Assess the morphology of the red blood cells.
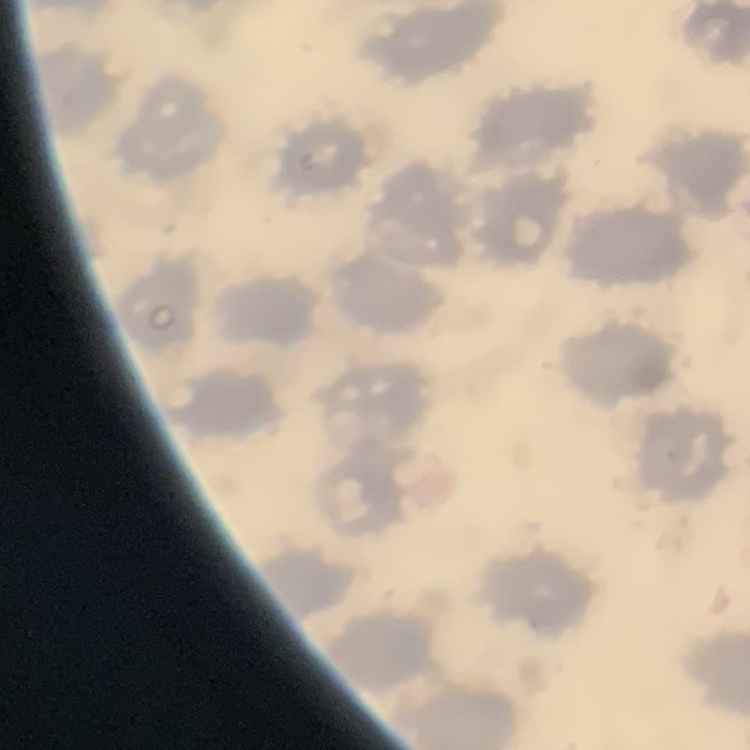

They show no rouleaux formation.

preparation = thin peripheral smear
stain = Field's or Giemsa
image type = square crop of a larger photomicrograph